Report the malaria status of this cell.
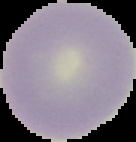

Uninfected.

Summary:
  - Preparation: thin blood film
  - Image size: 136×142 pixels
  - Image type: cell region segmented out of the field of view; surrounding area masked to black